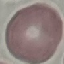

Summary:
  - Malaria status: uninfected
  - Capture: smartphone through the microscope eyepiece
  - Stain: Giemsa
  - Image type: automatically extracted cell patch, resized to 64 × 64 pixels
  - Preparation: thin blood smear